Comment on the morphology of the red blood cells.
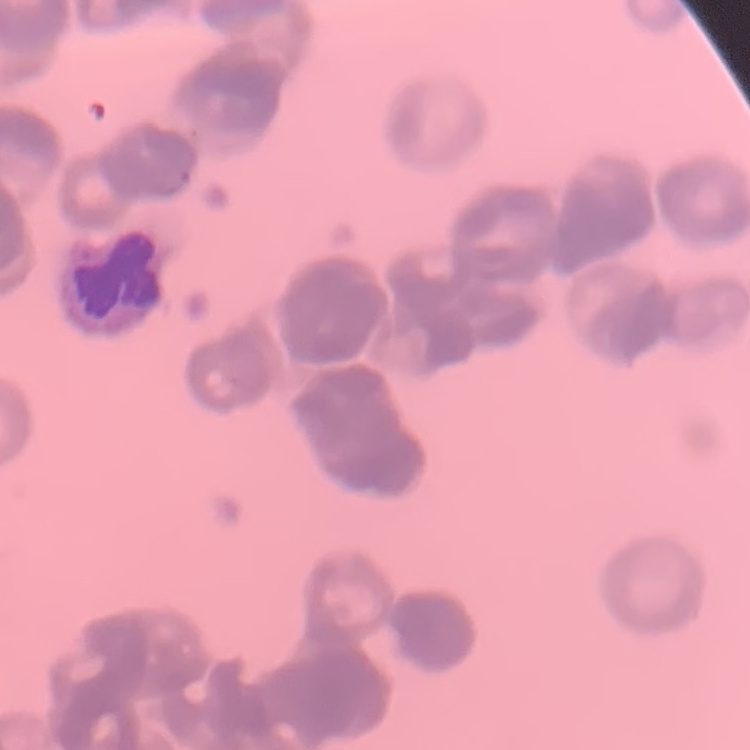

They show rouleaux formation.

preparation = thin peripheral smear
image type = one tile cut from a larger photomicrograph
stain = Field's or Giemsa